Report the malaria status of this cell.
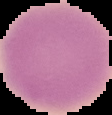
It is uninfected.

Summary:
  - Preparation: thin blood film
  - Image size: 112×115 pixels
  - Image type: segmented cell region with the area outside set to black